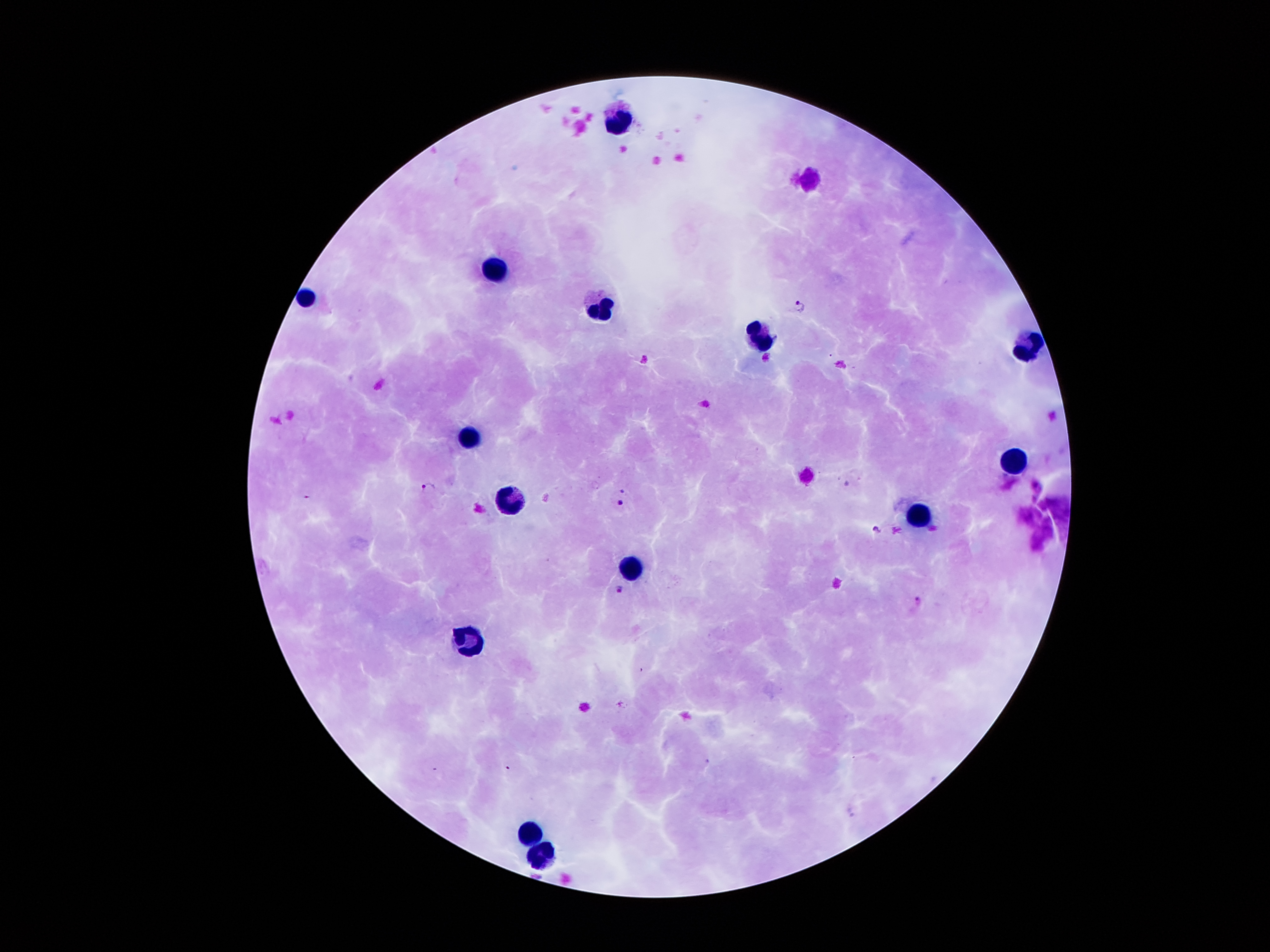 Approximate centers as (x, y) in pixels. Plasmodium parasite locations: (799, 303), (847, 484), (428, 487), (304, 495), (619, 502), (878, 530), (618, 589), (918, 600). Leukocyte locations: (620, 123), (499, 269), (307, 300), (601, 314), (756, 334), (1029, 352), (471, 437), (1017, 461), (508, 501), (919, 517), (628, 569), (467, 643), (528, 830), (538, 852). Image is 1270×952 pixels. Patient malaria status: infected with Plasmodium falciparum. Giemsa-stained preparation. 100x magnification. Thick blood smear. Photographed through the microscope eyepiece with a smartphone camera. Single field of view.